Classify this cell by malaria status.
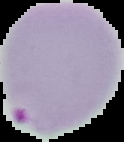

It is parasitized.

preparation = thin blood smear
image type = segmented cell region on a black background
image size = 124×142 pixels